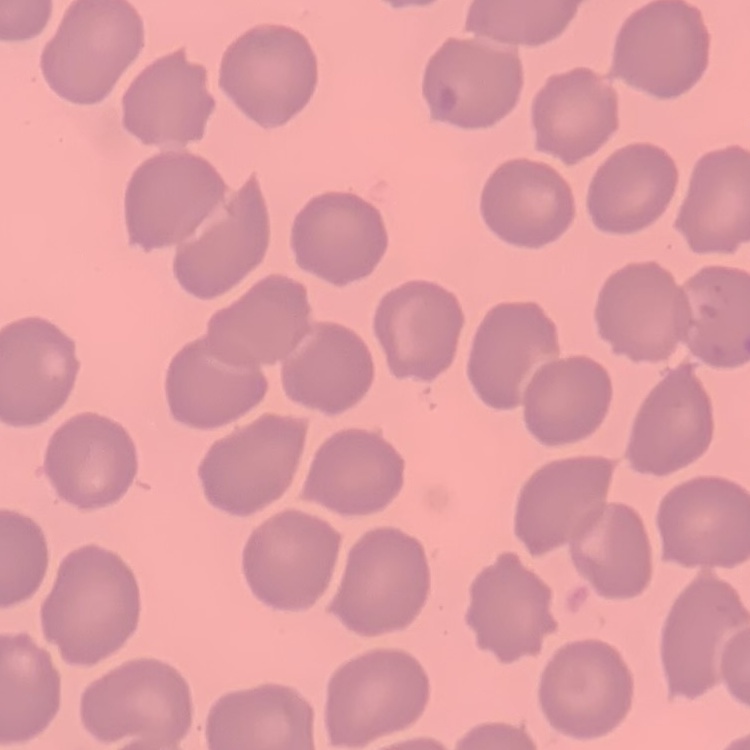 The red blood cells show no rouleaux formation. Field's or Giemsa stain. Square crop of a larger photomicrograph. Thin blood film.